Report the malaria status of this cell.
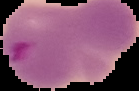

Parasitized.

Summary:
  - Image size: 139×91 pixels
  - Image type: segmented cell region with the area outside set to black
  - Preparation: thin blood film